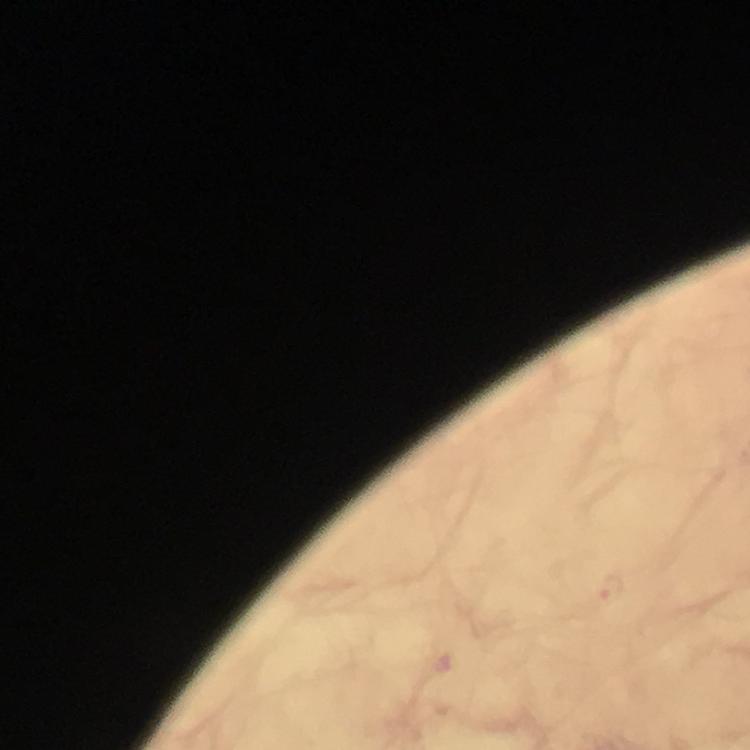
{
  "stain": "Giemsa",
  "preparation": "thick smear",
  "cropped_from": "one field of view",
  "image_size": "750×750 pixels",
  "magnification": "100x",
  "immersion_oil": "used",
  "malaria_parasite_locations": "approximate object centers, in pixels from the top-left corner: (x=611, y=588)",
  "capture": "smartphone camera through the microscope",
  "context": "from a malaria diagnostic workup"
}